Assess for Plasmodium parasites.
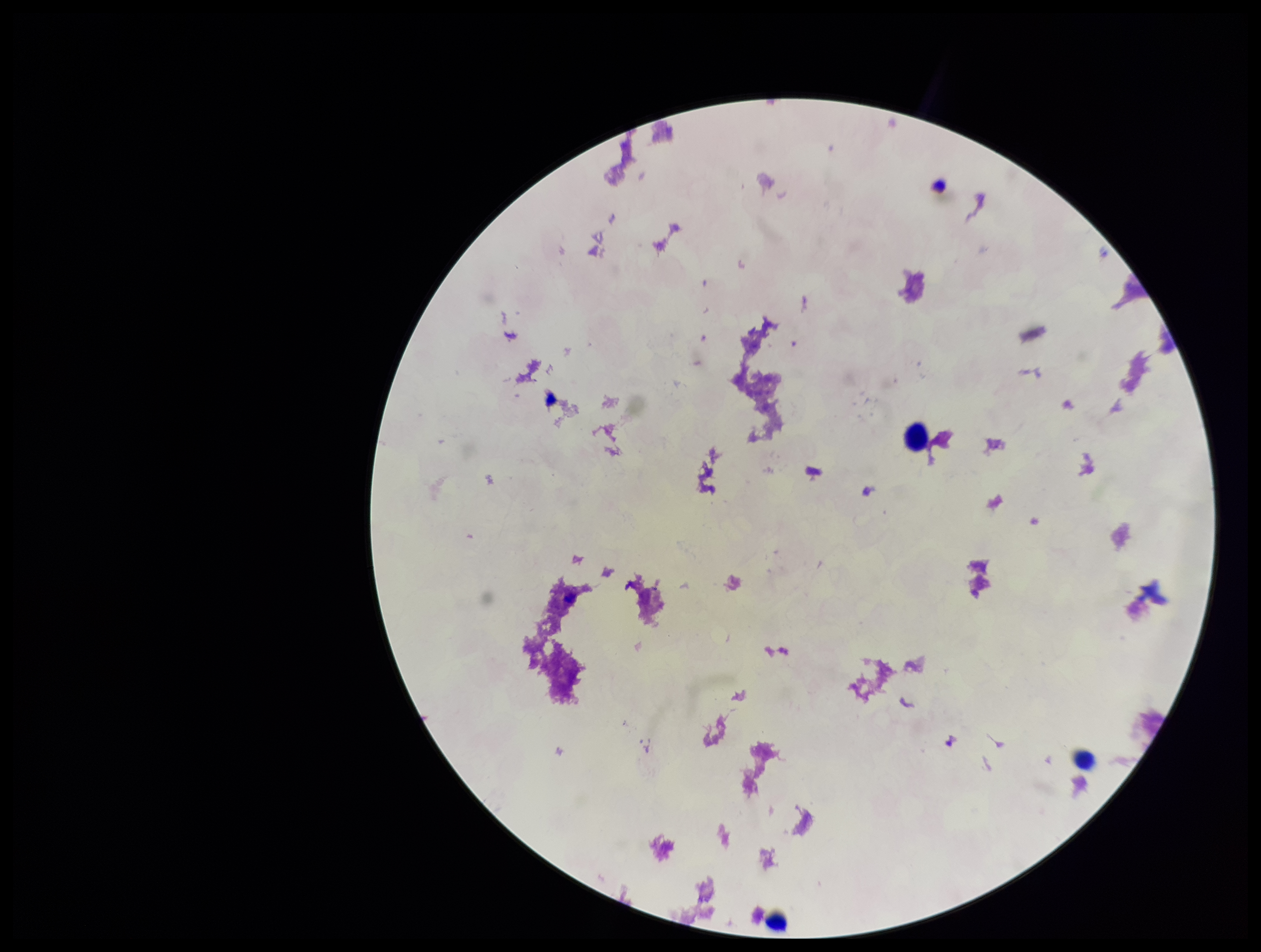
None seen.

One field from this slide. Preparation: thick. Patient malaria status: negative. Parasite count: 0. Stained with Giemsa. Smartphone photograph taken through the eyepiece of a microscope. Image is 1261×952 pixels. Leukocyte count: 3.